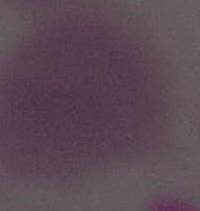

modality: micrograph
magnification: 1000x
identification: red blood cell